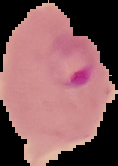
Summary:
  - Image size: 118×166 pixels
  - Preparation: thin blood smear
  - Result: Plasmodium parasites identified
  - Image type: cell region segmented out of the field of view; surrounding area masked to black